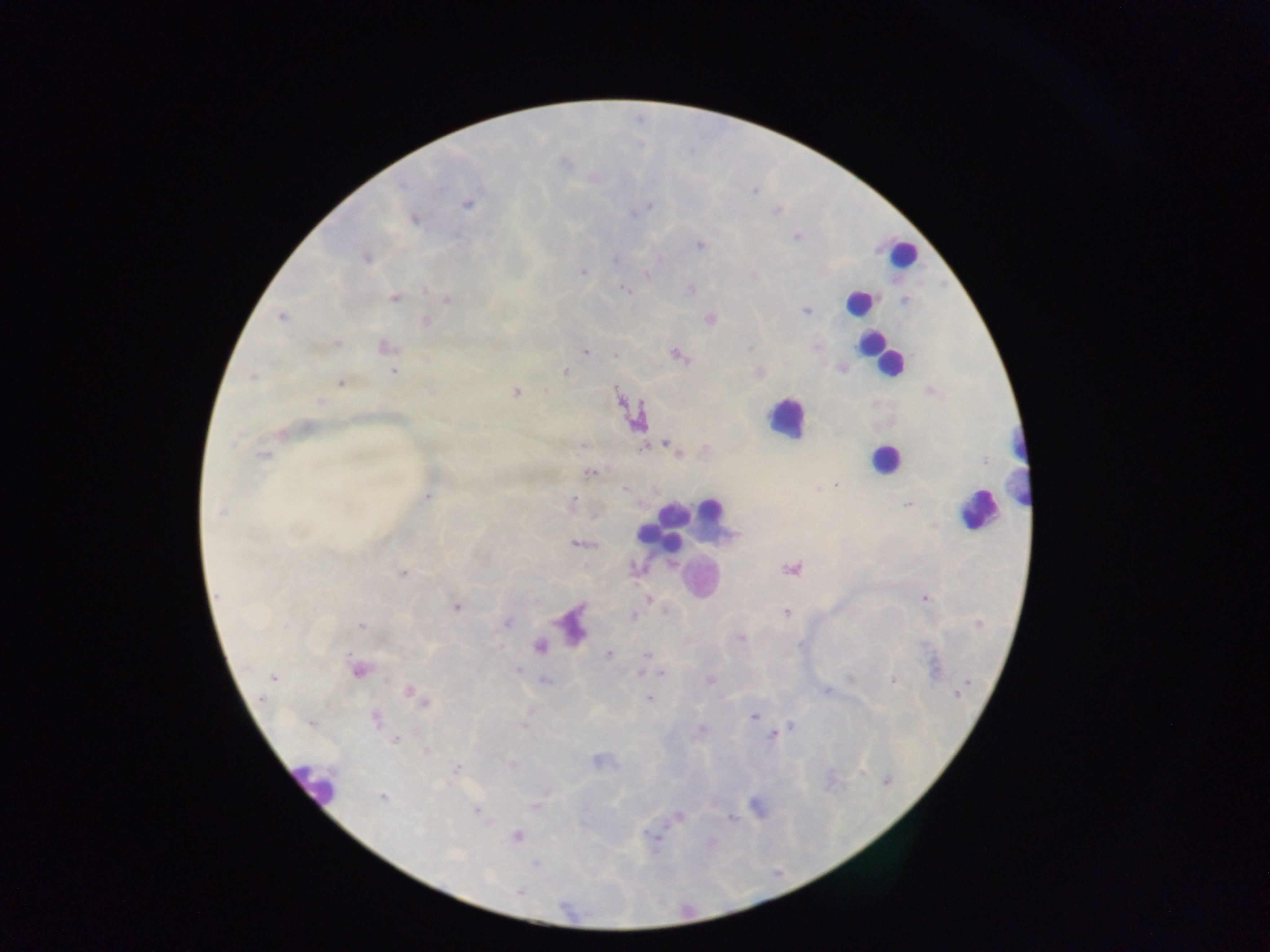 Approximate centers as (x, y) in pixels. Plasmodium parasite locations: (754, 191), (467, 205), (646, 206), (776, 211), (634, 214), (414, 220), (700, 245), (367, 258), (615, 259), (583, 272), (647, 274), (623, 289), (691, 289), (394, 298), (447, 299), (806, 310), (282, 318), (710, 319), (426, 322), (337, 343), (386, 346), (750, 347), (817, 347), (585, 351), (615, 354), (677, 355), (394, 372), (564, 372), (760, 372), (252, 377), (340, 383), (516, 392), (320, 403), (307, 427), (281, 432), (583, 445), (670, 446), (643, 448), (678, 453), (262, 455), (590, 472), (835, 484), (625, 490), (428, 496), (573, 501), (908, 504), (220, 513), (578, 544), (635, 568), (791, 568), (402, 573), (925, 598), (649, 599), (456, 606), (786, 612), (633, 616), (507, 623), (287, 625), (360, 625), (741, 637), (799, 644), (539, 646), (608, 654), (647, 655), (359, 670), (517, 670), (641, 672), (662, 673), (273, 677), (893, 680), (546, 681), (709, 681), (826, 691), (410, 693), (958, 693), (262, 698), (649, 699), (424, 702), (754, 715), (375, 719), (311, 723), (790, 726), (702, 729), (772, 735), (395, 740), (427, 750), (457, 768), (888, 781), (383, 798), (535, 807), (478, 811), (679, 817), (731, 818), (517, 836), (652, 836), (535, 864), (519, 892). Leukocyte locations: (901, 253), (858, 302), (880, 355), (785, 419), (884, 459), (1020, 462), (976, 509), (712, 510), (673, 513), (668, 523), (652, 535), (314, 782). Photographed through a microscope with a mobile-phone camera. Collected in Ghana. Single field of view. Image is 1270×952 pixels. Thick blood smear.